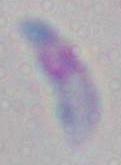

magnification = 1000x
identification = Toxoplasma gondii
modality = photomicrograph